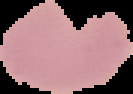

image type = cell region segmented out of the field of view; surrounding area masked to black
image size = 133×94 pixels
result = negative for Plasmodium parasites
preparation = thin blood film